Evaluate for Plasmodium parasites.
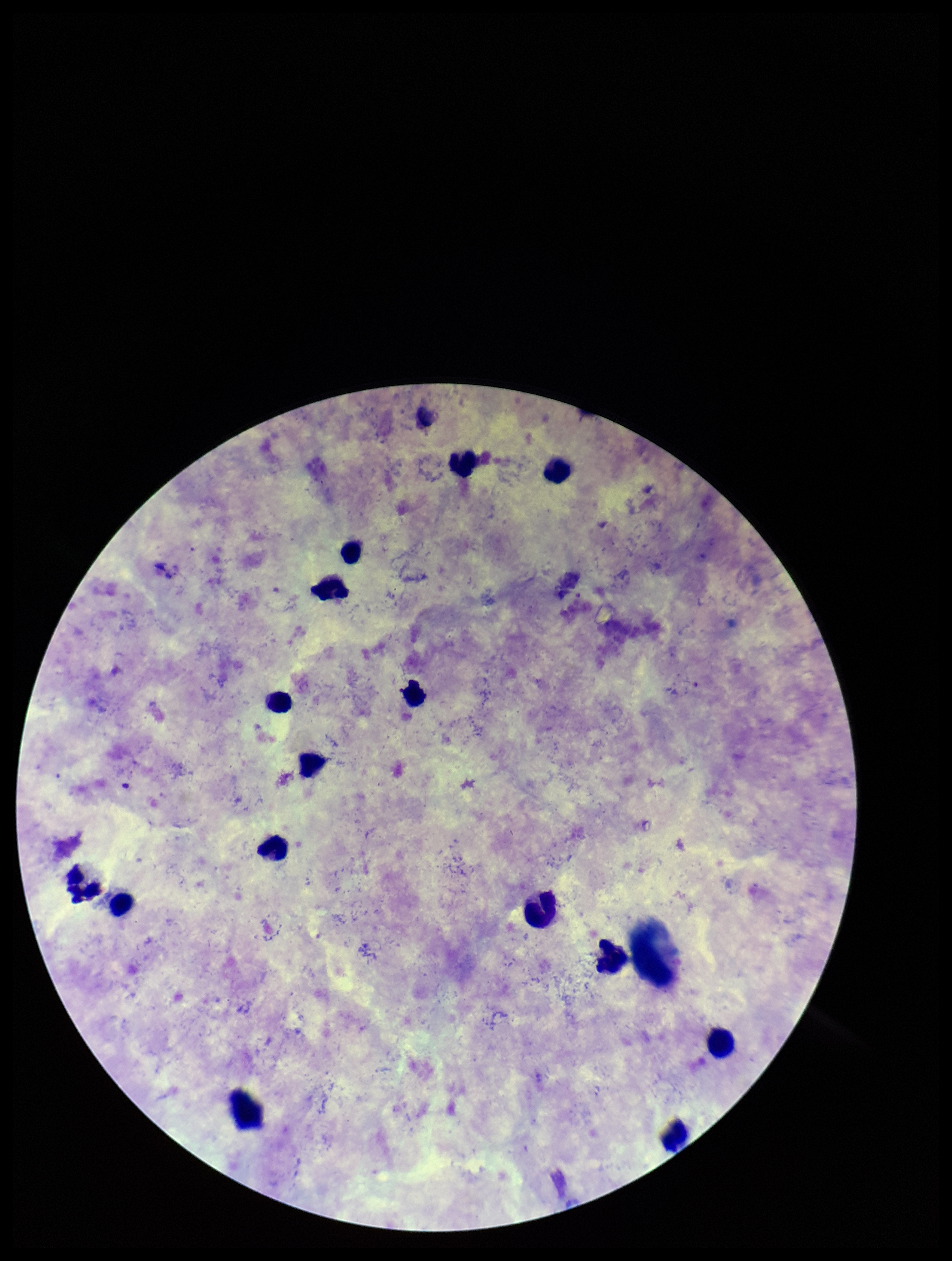
None detected.

Summary:
  - Patient malaria status: infected
  - Leukocyte count: 15
  - Stain: Giemsa
  - Parasite count: 0
  - Image size: 952×1261 pixels
  - Preparation: thick smear
  - Field of view: single
  - Species reported for this patient: Plasmodium vivax
  - Capture: smartphone photograph through the microscope eyepiece